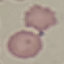
result = negative for malaria parasites
preparation = thin blood film
stain = Giemsa
image type = automatically extracted cell patch, resized to 64 × 64 pixels
capture = smartphone camera at the microscope eyepiece